Locate every blood parasite and identify its species.
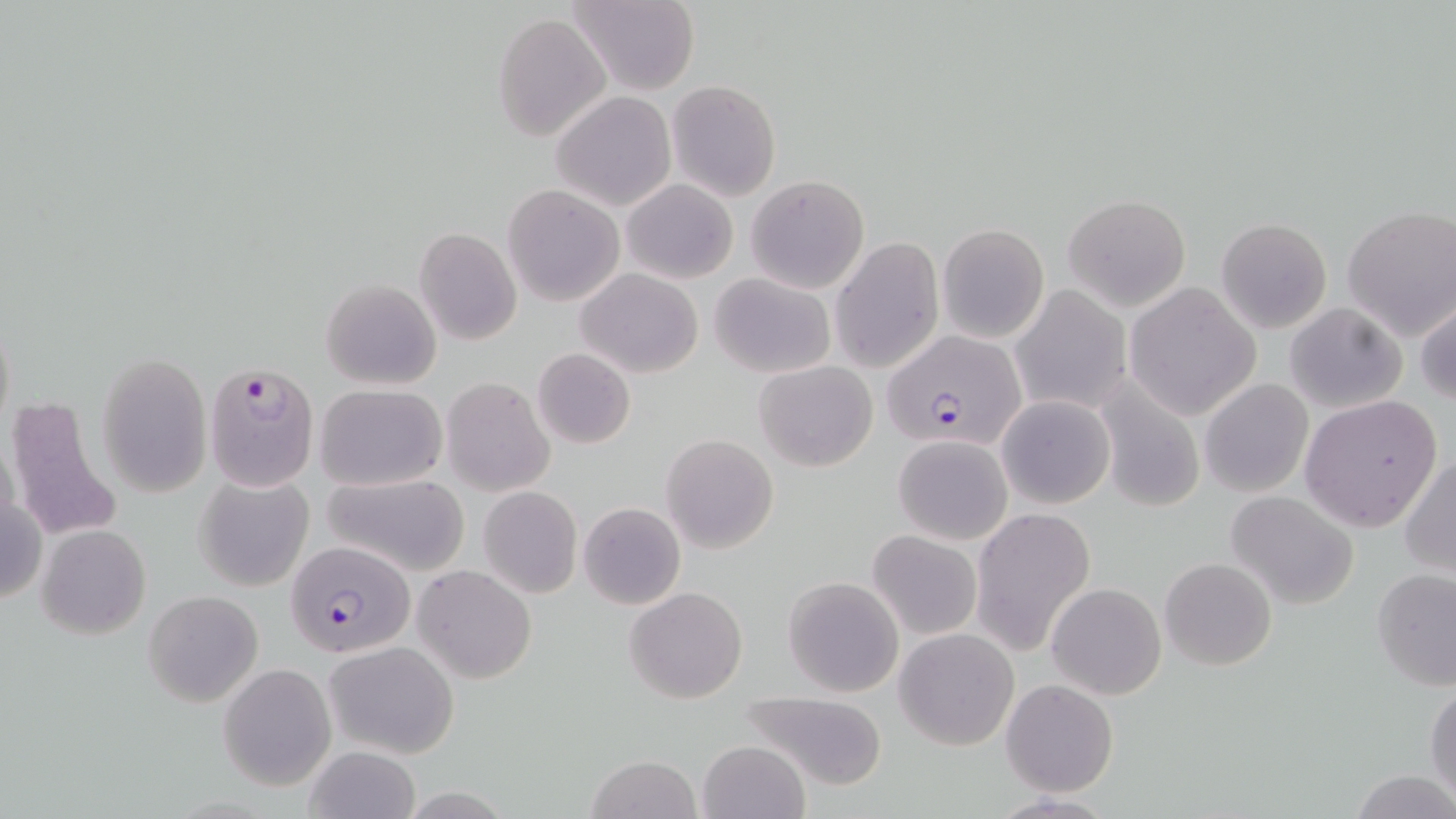

Approximate bounding boxes as named x1/y1/x2/y2 corners in pixels.
Plasmodium falciparum-infected red blood cells: (x1=882, y1=328, x2=1028, y2=449), (x1=204, y1=362, x2=320, y2=491), (x1=287, y1=542, x2=415, y2=658).
No Plasmodium ovale, Plasmodium malariae, Plasmodium vivax, Babesia divergens, or Trypanosoma brucei observed.

Summary:
  - Uninfected red blood cell locations: (x1=567, y1=0, x2=700, y2=94), (x1=493, y1=12, x2=610, y2=142), (x1=667, y1=80, x2=781, y2=201), (x1=551, y1=90, x2=676, y2=210), (x1=745, y1=173, x2=870, y2=294), (x1=622, y1=178, x2=737, y2=283), (x1=503, y1=185, x2=624, y2=307), (x1=1064, y1=194, x2=1189, y2=312), (x1=1341, y1=205, x2=1456, y2=342), (x1=1216, y1=217, x2=1332, y2=335), (x1=937, y1=223, x2=1049, y2=344), (x1=414, y1=227, x2=522, y2=346), (x1=831, y1=238, x2=943, y2=373), (x1=576, y1=267, x2=703, y2=378), (x1=709, y1=272, x2=836, y2=379), (x1=320, y1=279, x2=441, y2=390), (x1=1123, y1=283, x2=1261, y2=421), (x1=1013, y1=285, x2=1130, y2=412), (x1=1415, y1=295, x2=1456, y2=408), (x1=1284, y1=302, x2=1408, y2=414), (x1=533, y1=347, x2=636, y2=449), (x1=96, y1=352, x2=211, y2=498), (x1=755, y1=359, x2=876, y2=472), (x1=1094, y1=375, x2=1207, y2=513), (x1=441, y1=377, x2=556, y2=496), (x1=1199, y1=378, x2=1314, y2=499), (x1=316, y1=384, x2=446, y2=491), (x1=6, y1=394, x2=125, y2=545), (x1=998, y1=394, x2=1114, y2=509), (x1=1300, y1=394, x2=1443, y2=532), (x1=661, y1=434, x2=778, y2=552), (x1=892, y1=434, x2=1013, y2=544), (x1=1401, y1=453, x2=1456, y2=577), (x1=1, y1=470, x2=44, y2=611), (x1=321, y1=472, x2=470, y2=577), (x1=193, y1=473, x2=315, y2=592), (x1=477, y1=485, x2=582, y2=598), (x1=1227, y1=491, x2=1359, y2=610), (x1=579, y1=502, x2=685, y2=609), (x1=970, y1=507, x2=1094, y2=658), (x1=36, y1=525, x2=151, y2=641), (x1=868, y1=531, x2=981, y2=640), (x1=1160, y1=557, x2=1276, y2=671), (x1=414, y1=564, x2=537, y2=683), (x1=1372, y1=569, x2=1456, y2=693), (x1=782, y1=575, x2=905, y2=698), (x1=1046, y1=582, x2=1165, y2=700), (x1=624, y1=586, x2=748, y2=703), (x1=143, y1=590, x2=263, y2=708), (x1=895, y1=628, x2=1018, y2=750), (x1=324, y1=640, x2=460, y2=758), (x1=218, y1=663, x2=335, y2=791), (x1=1001, y1=680, x2=1118, y2=798), (x1=1426, y1=682, x2=1456, y2=802), (x1=738, y1=690, x2=889, y2=793), (x1=697, y1=739, x2=808, y2=819), (x1=300, y1=746, x2=420, y2=819), (x1=585, y1=755, x2=700, y2=818), (x1=1350, y1=770, x2=1455, y2=819)
  - Slide-level diagnosis: Plasmodium falciparum
  - Field of view: one of a larger specimen
  - Image size: 1456×819 pixels
  - Preparation: thin blood smear
  - Magnification: 1000x
  - Stain: May-Grünwald-Giemsa
  - Modality: light microscopy